Locate every blood parasite and identify its species.
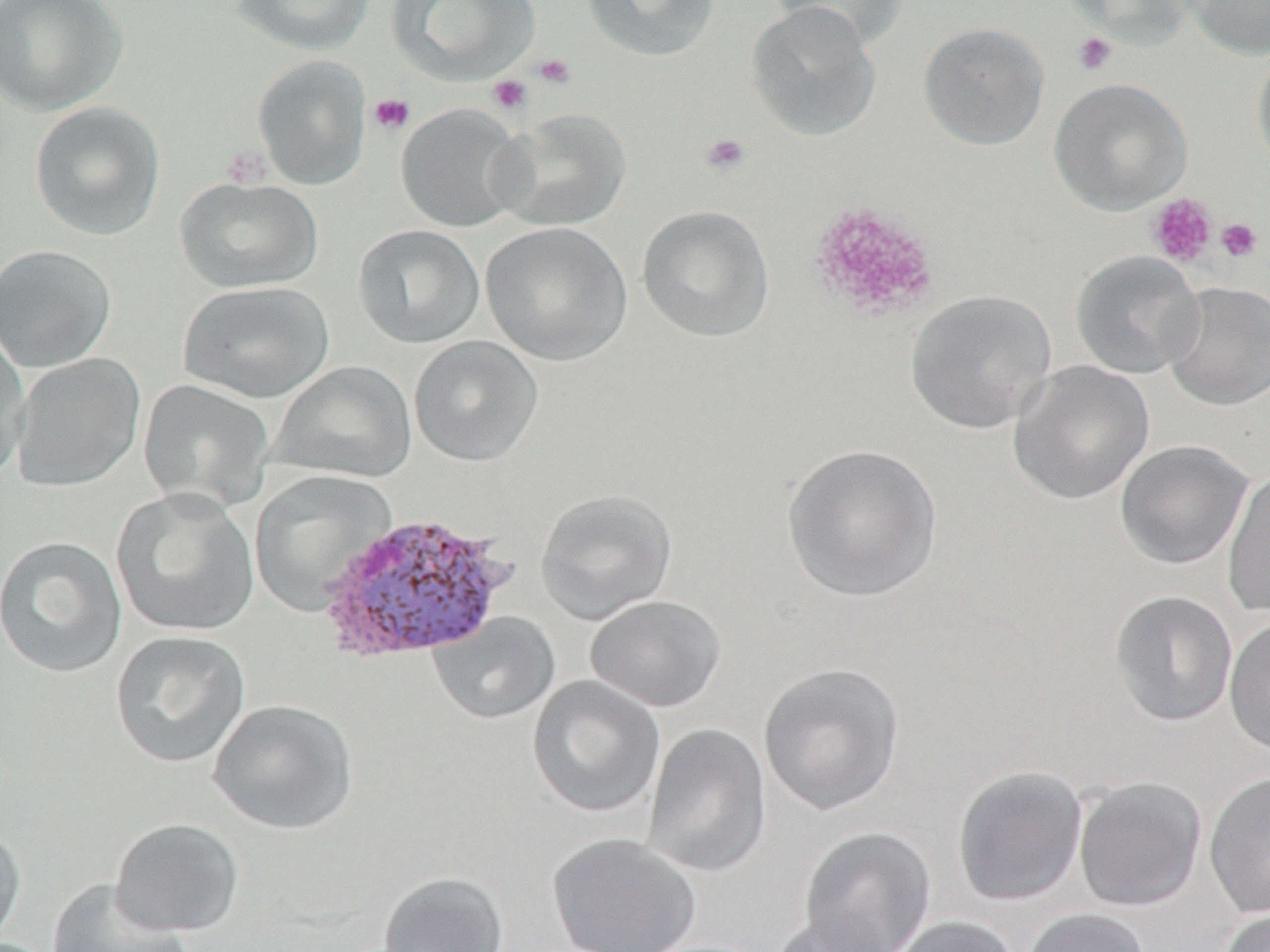
Approximate bounding boxes as (x1, y1, x2, y2) in pixels.
Plasmodium vivax-infected red blood cells: (317, 511, 516, 663).
No Plasmodium falciparum, Plasmodium ovale, Plasmodium malariae, Babesia divergens, or Trypanosoma brucei observed.

slide-level diagnosis = Plasmodium vivax
modality = light microscopy
magnification = 1000x
platelet locations = approximate bounding boxes as (x1, y1, x2, y2) in pixels: (1071, 32, 1117, 76), (533, 53, 576, 89), (487, 74, 533, 116), (368, 93, 415, 136), (700, 132, 750, 176), (221, 145, 271, 188), (1145, 193, 1218, 268), (808, 201, 940, 321), (1215, 217, 1263, 263)
preparation = thin blood film
image size = 1270×952 pixels
field of view = one of a larger specimen
uninfected red blood cell locations = approximate bounding boxes as (x1, y1, x2, y2) in pixels: (0, 0, 128, 117), (231, 0, 376, 56), (387, 0, 540, 84), (581, 0, 720, 63), (769, 0, 908, 51), (1065, 0, 1195, 49), (1182, 0, 1270, 60), (745, 3, 881, 141), (917, 21, 1050, 150), (1251, 48, 1270, 176), (252, 55, 372, 191), (1048, 77, 1192, 216), (29, 101, 166, 240), (395, 103, 528, 232), (493, 109, 631, 231), (174, 175, 323, 294), (636, 204, 774, 342), (480, 221, 632, 366), (352, 223, 486, 349), (0, 244, 118, 372), (1070, 250, 1205, 379), (177, 280, 335, 404), (1162, 281, 1270, 411), (905, 290, 1056, 434), (0, 327, 31, 480), (409, 335, 543, 466), (9, 352, 145, 494), (1008, 360, 1156, 505), (269, 361, 417, 484), (138, 378, 275, 511), (1115, 439, 1254, 570), (781, 443, 943, 601), (1222, 469, 1270, 619), (249, 470, 395, 615), (111, 487, 260, 637), (535, 488, 678, 623), (1, 535, 129, 678), (1109, 589, 1238, 727), (585, 595, 727, 713), (428, 612, 561, 725), (1224, 613, 1270, 756), (110, 630, 251, 768), (758, 662, 905, 816), (527, 675, 666, 818), (207, 699, 358, 835), (642, 722, 772, 878), (952, 765, 1088, 907), (1203, 770, 1270, 919), (1073, 777, 1208, 911), (109, 817, 245, 938), (0, 821, 26, 947), (798, 826, 937, 952), (547, 832, 702, 952), (377, 871, 510, 952), (46, 878, 193, 952), (1021, 907, 1153, 952), (1215, 907, 1269, 952), (767, 913, 898, 952), (886, 916, 1021, 952)
stain = May-Grünwald-Giemsa